Outline every artifact (stain precipitate or debris).
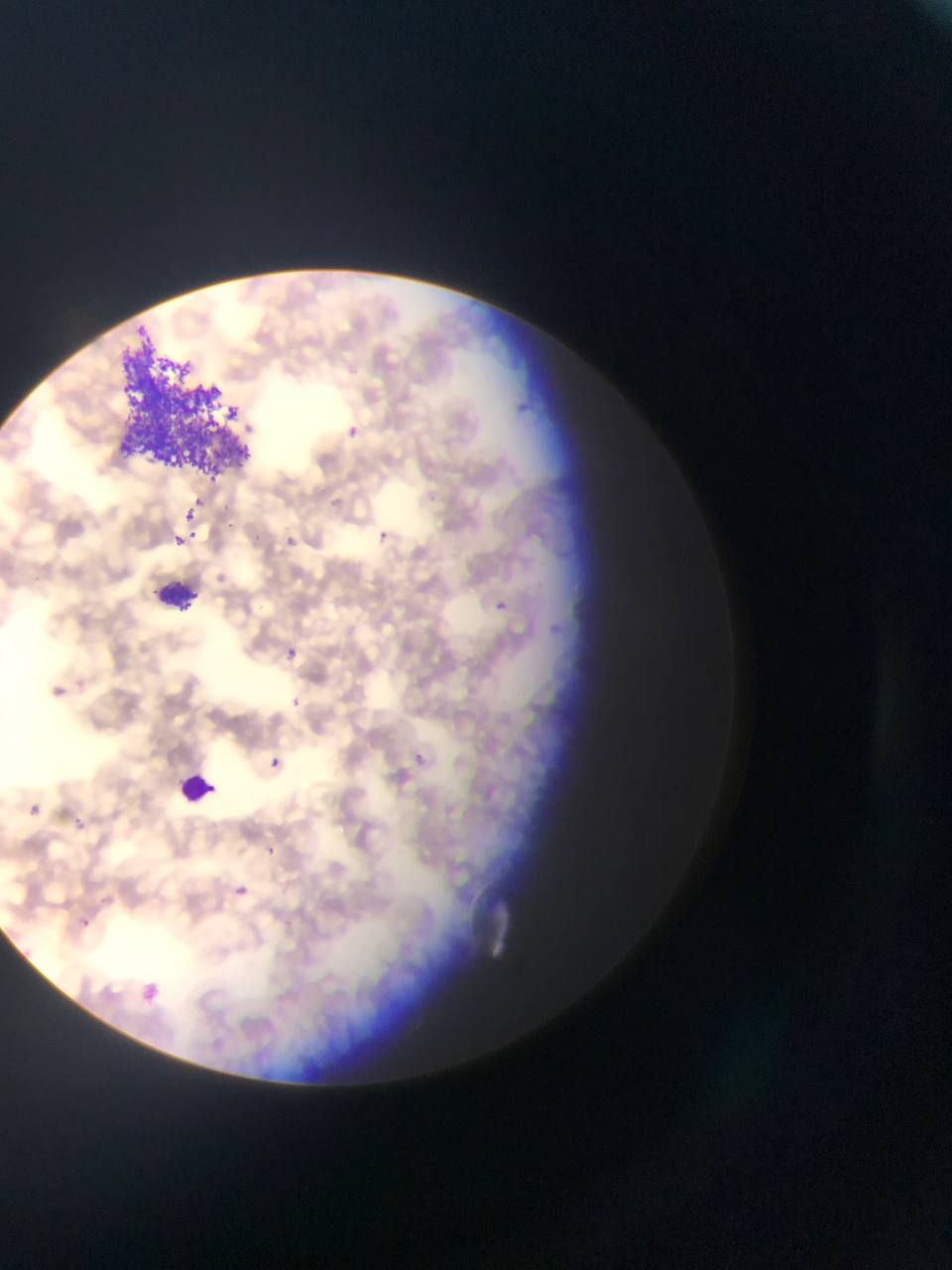

Approximate bounding boxes as left top right bottom in pixels.
Artifacts (stain precipitate or debris): 126 323 254 475.

Malaria parasite locations: 514 395 531 421; 344 419 363 442; 192 486 209 509; 184 508 198 523; 225 519 238 532; 182 525 201 539; 376 526 395 550; 171 532 185 545; 284 535 297 547; 495 599 509 611; 283 646 296 661; 288 694 305 714; 268 754 281 774; 413 754 425 770; 28 804 42 817; 71 813 91 826; 265 845 281 858; 236 885 249 895; 77 910 103 929; 142 982 162 1004. One field of view. Mobile-phone photograph taken through the microscope. Sample from Ghana. Thin blood smear. Image is 952×1270 pixels.